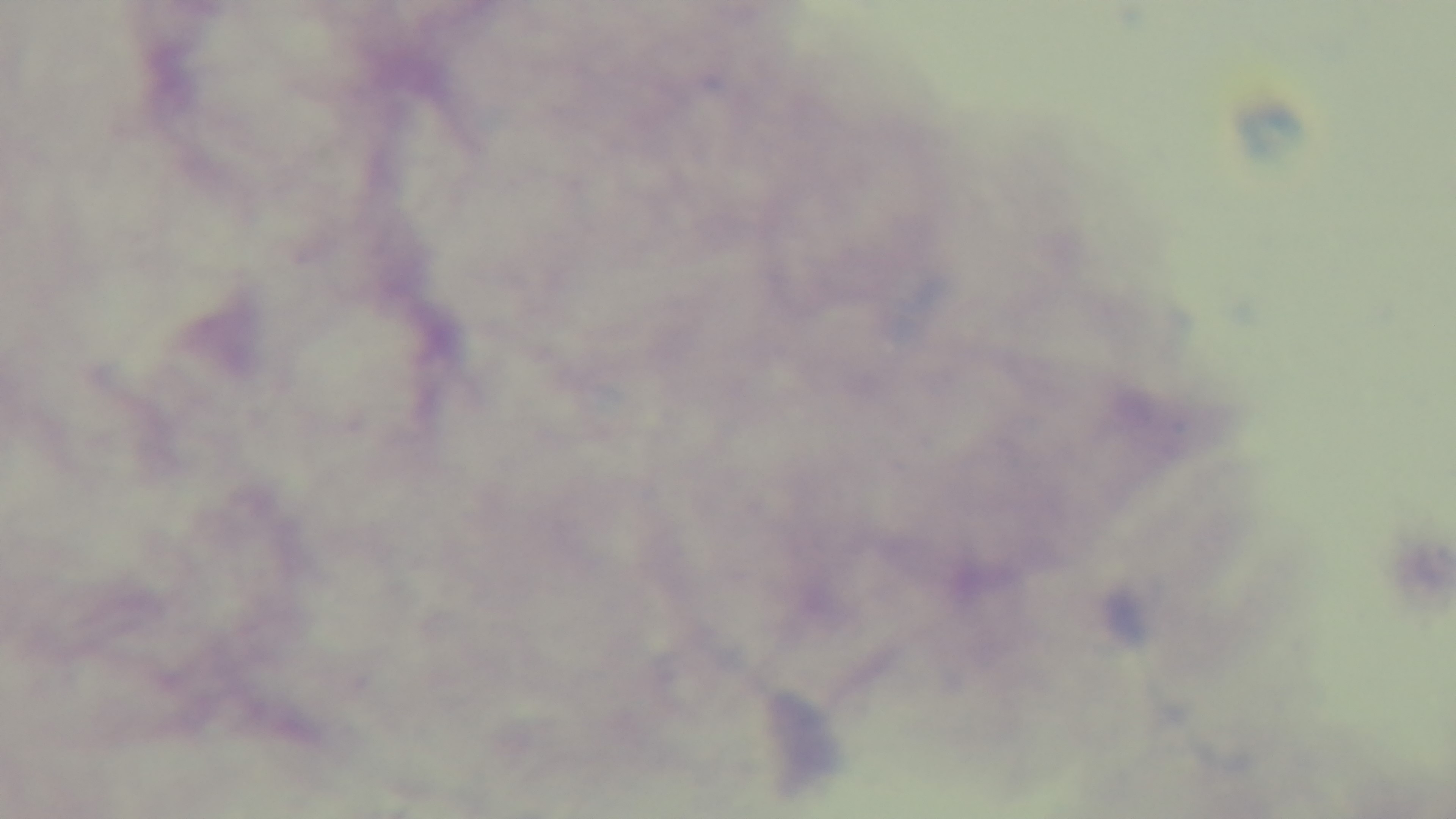 Mounted 4K digital camera. Photomicrograph. Oil-immersion objective, 100x. Single field of view. Giemsa stain. Malaria status: negative. Preparation: thick smear.